Comment on the morphology of the erythrocytes.
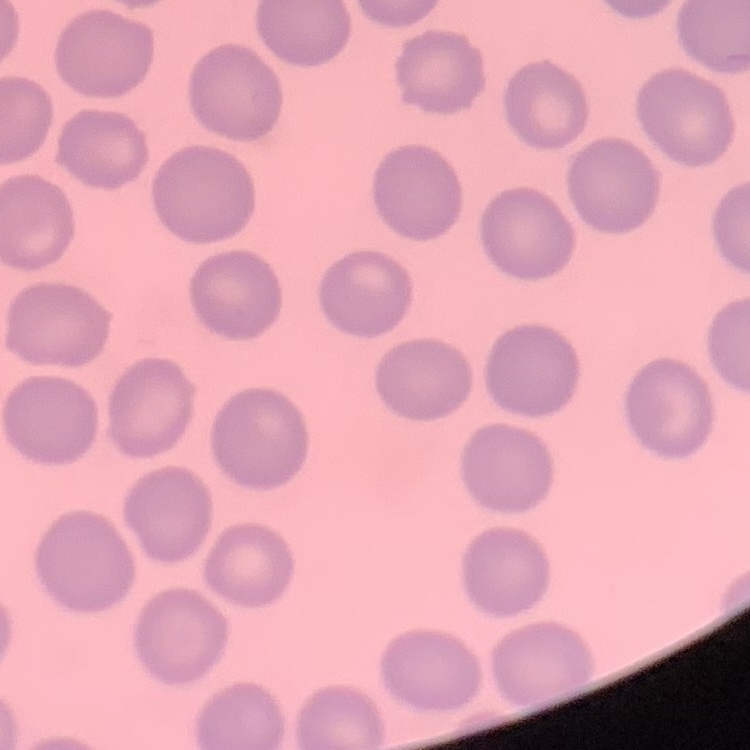
They show no rouleaux formation.

{
  "preparation": "thin blood film",
  "stain": "Field's or Giemsa",
  "image_type": "square crop of a larger photomicrograph"
}